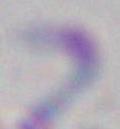
Toxoplasma gondii is seen. Captured at 1000x magnification. Photomicrograph.